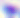

400x magnification. Toxoplasma gondii is seen. Photomicrograph.